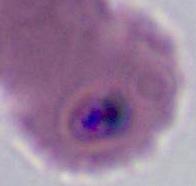
identification = Plasmodium
magnification = 400x or 1000x
modality = photomicrograph